Name the cell type shown.
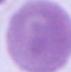
An erythrocyte.

Captured at 1000x magnification. Photomicrograph.